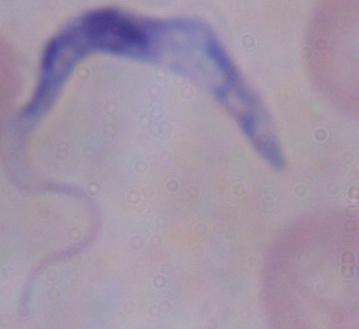
Summary:
  - Modality: photomicrograph
  - Identification: trypanosome
  - Magnification: 1000x